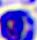

magnification = 400x
modality = micrograph
identification = leukocyte